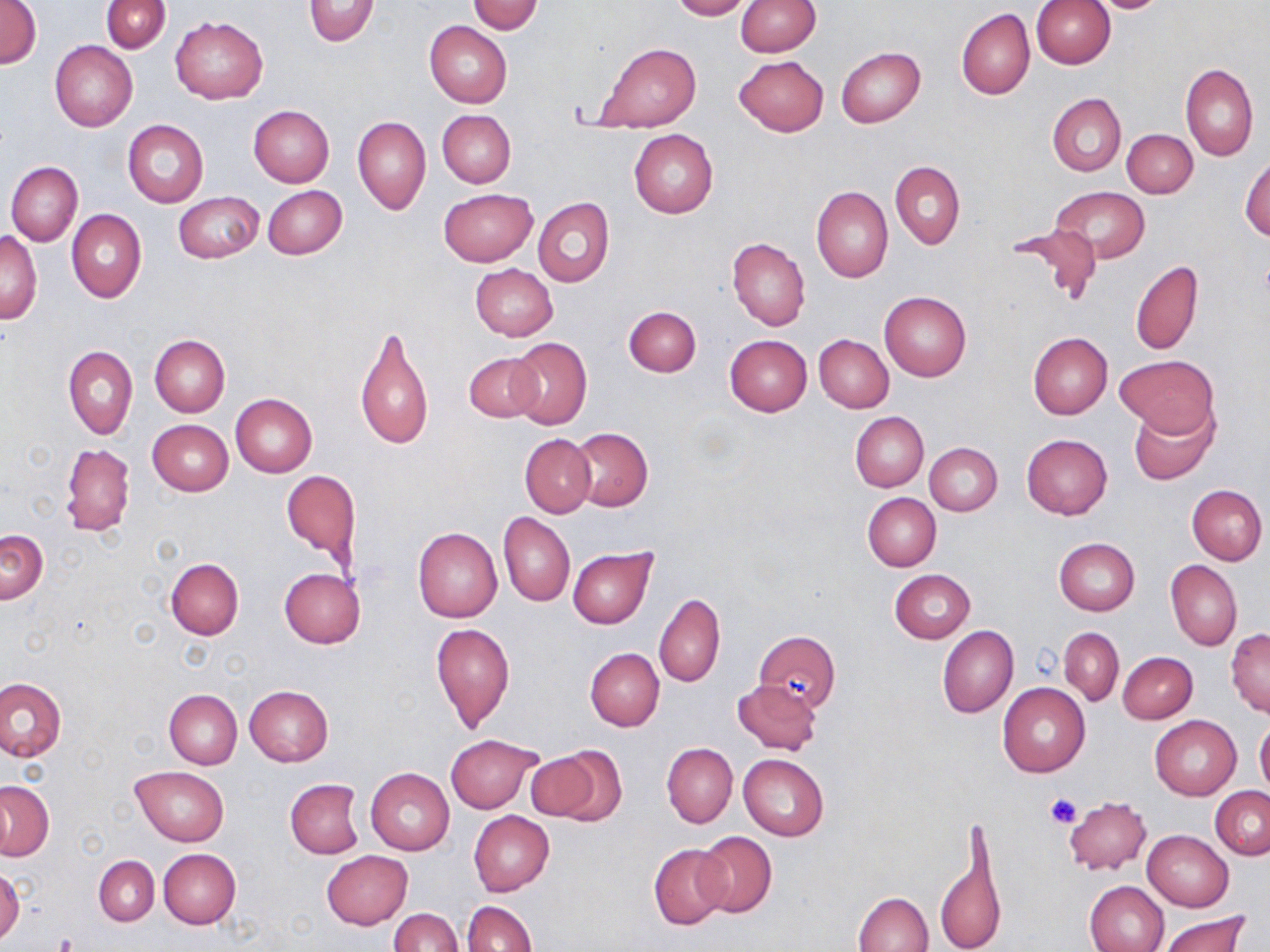 Approximate bounding boxes as [x1, y1, x2, y2] in pixels. Platelet locations: [1046, 793, 1083, 830], [54, 932, 77, 951]. Uninfected red blood cell locations: [101, 0, 170, 54], [302, 0, 379, 46], [669, 0, 750, 20], [1089, 0, 1173, 13], [1, 1, 42, 70], [469, 1, 544, 35], [736, 1, 819, 57], [1031, 1, 1115, 68], [959, 6, 1114, 85], [956, 8, 1035, 99], [170, 16, 267, 103], [424, 21, 511, 109], [50, 41, 137, 131], [596, 43, 699, 134], [836, 47, 925, 127], [734, 55, 829, 136], [1180, 64, 1258, 160], [1047, 92, 1126, 176], [249, 105, 334, 187], [438, 110, 516, 187], [352, 115, 430, 214], [123, 119, 209, 208], [1122, 128, 1198, 198], [628, 129, 717, 218], [1240, 155, 1269, 241], [5, 161, 83, 246], [891, 161, 965, 250], [263, 184, 348, 259], [811, 185, 893, 282], [1050, 186, 1151, 262], [438, 187, 537, 266], [174, 191, 263, 264], [533, 197, 613, 287], [66, 209, 146, 303], [1013, 223, 1105, 306], [2, 231, 41, 323], [727, 238, 811, 330], [1130, 259, 1204, 355], [469, 264, 557, 341], [879, 291, 971, 381], [623, 306, 701, 376], [354, 322, 434, 452], [1027, 332, 1112, 419], [813, 334, 894, 413], [149, 335, 229, 416], [724, 335, 811, 416], [506, 337, 592, 429], [63, 345, 137, 439], [465, 352, 543, 422], [1115, 354, 1220, 439], [230, 394, 317, 477], [1129, 403, 1216, 484], [850, 411, 928, 492], [148, 420, 233, 496], [569, 427, 652, 511], [1021, 433, 1113, 519], [521, 434, 595, 516], [925, 442, 1002, 515], [61, 444, 134, 538], [282, 470, 361, 567], [1187, 484, 1267, 565], [862, 492, 940, 570], [498, 512, 574, 606], [413, 527, 502, 622], [1, 528, 48, 604], [1054, 537, 1140, 614], [568, 548, 657, 629], [165, 558, 243, 639], [1165, 560, 1242, 651], [278, 568, 365, 648], [889, 569, 975, 643], [655, 594, 725, 687], [430, 622, 515, 732], [937, 624, 1019, 719], [1058, 628, 1124, 704], [1226, 628, 1270, 716], [753, 631, 840, 711], [584, 648, 664, 731], [1117, 652, 1197, 724], [0, 677, 65, 761], [733, 679, 822, 755], [997, 682, 1091, 777], [245, 686, 333, 766], [164, 689, 241, 769], [1150, 714, 1241, 799], [1254, 719, 1270, 796], [446, 734, 542, 812], [662, 743, 737, 827], [539, 746, 627, 825], [739, 753, 828, 842], [131, 765, 229, 845], [366, 768, 454, 854], [285, 779, 363, 858], [0, 781, 53, 859], [1211, 786, 1270, 859], [1063, 796, 1151, 875], [469, 811, 555, 895], [1142, 829, 1233, 911], [693, 831, 777, 918], [935, 833, 1002, 952], [649, 844, 730, 929], [159, 849, 240, 928], [322, 850, 412, 928], [94, 856, 159, 925], [0, 868, 23, 948], [1084, 879, 1169, 952], [854, 891, 934, 952], [463, 900, 536, 952], [388, 908, 462, 952], [1158, 911, 1250, 952]. Slide-level diagnosis: no evidence of blood parasites. Single field of view. Image is 1270×952 pixels. Light microscopy. May-Grünwald-Giemsa stain. 1000x magnification. Thin blood smear.